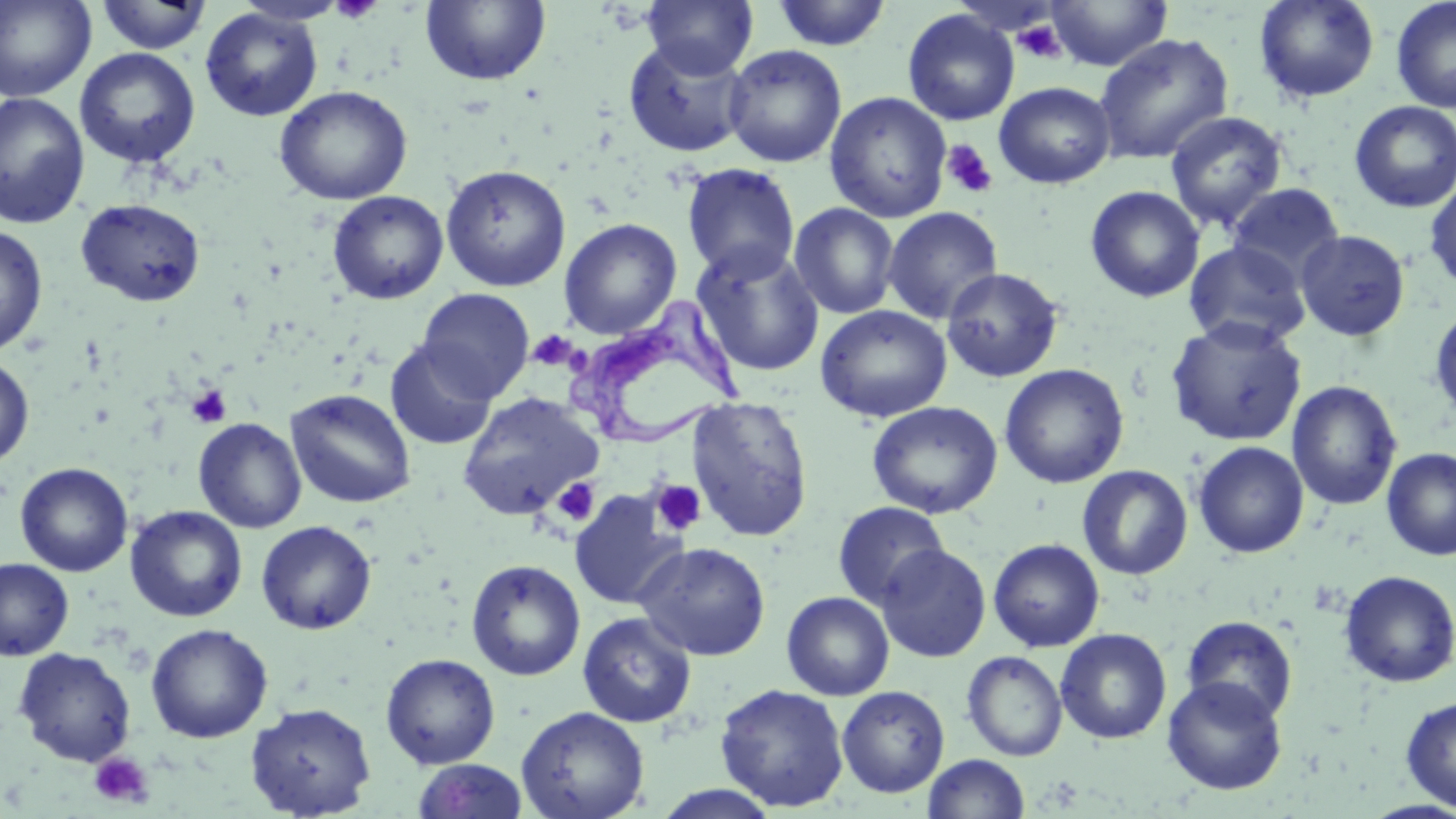
slide-level diagnosis = Trypanosoma brucei
field of view = single
modality = light microscopy
uninfected red blood cell locations = approximate bounding boxes as [x1, y1, x2, y2] in pixels: [0, 0, 97, 102], [642, 0, 758, 78], [1045, 0, 1173, 71], [1254, 0, 1380, 103], [1390, 0, 1456, 114], [94, 1, 213, 55], [420, 1, 551, 87], [769, 1, 893, 51], [200, 8, 323, 122], [902, 9, 1019, 126], [1093, 33, 1234, 164], [623, 38, 752, 158], [723, 45, 847, 168], [74, 48, 200, 168], [994, 82, 1116, 188], [273, 85, 412, 205], [0, 92, 90, 229], [824, 92, 952, 223], [1349, 101, 1456, 213], [1164, 111, 1288, 233], [681, 162, 801, 282], [440, 164, 572, 292], [1425, 177, 1456, 291], [1226, 182, 1345, 285], [1085, 185, 1205, 303], [327, 190, 449, 304], [76, 198, 206, 307], [789, 203, 900, 319], [883, 206, 1003, 325], [559, 217, 682, 339], [0, 225, 48, 357], [1295, 229, 1410, 342], [1184, 240, 1310, 350], [692, 244, 825, 378], [941, 267, 1064, 383], [417, 288, 534, 401], [1429, 304, 1456, 423], [816, 305, 952, 422], [1165, 317, 1307, 447], [385, 340, 497, 450], [0, 354, 34, 467], [1000, 363, 1129, 489], [1287, 380, 1401, 510], [284, 388, 417, 509], [456, 391, 603, 520], [686, 396, 814, 542], [867, 401, 1003, 519], [193, 417, 307, 533], [1192, 441, 1309, 558], [1381, 448, 1456, 561], [16, 462, 133, 576], [1077, 465, 1193, 580], [568, 490, 686, 610], [831, 501, 951, 609], [125, 505, 248, 622], [127, 514, 377, 625], [255, 520, 377, 635], [988, 538, 1105, 652], [635, 541, 771, 661], [876, 544, 991, 662], [0, 558, 74, 660], [466, 559, 586, 681], [1339, 570, 1456, 688], [781, 591, 895, 701], [577, 611, 697, 727], [1181, 615, 1298, 723], [145, 623, 273, 743], [1055, 628, 1172, 744], [13, 647, 136, 767], [962, 651, 1068, 761], [380, 653, 501, 769], [1162, 676, 1288, 795], [715, 683, 850, 812], [836, 685, 950, 798], [1400, 696, 1456, 811], [244, 701, 376, 818], [515, 706, 650, 819], [922, 753, 1030, 819], [412, 759, 529, 818], [648, 786, 784, 819]
magnification = 1000x
preparation = thin blood film
image size = 1456×819 pixels
stain = May-Grünwald-Giemsa
platelet locations = approximate bounding boxes as [x1, y1, x2, y2] in pixels: [329, 0, 382, 23], [1013, 19, 1067, 63], [940, 139, 999, 199], [534, 331, 574, 367], [187, 384, 232, 428], [551, 477, 601, 527], [649, 479, 707, 537], [89, 752, 154, 808]
Trypanosoma brucei locations = approximate bounding boxes as [x1, y1, x2, y2] in pixels: [569, 306, 742, 450]